State which parasite is depicted.
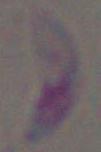
This is Toxoplasma gondii.

Summary:
  - Magnification: 1000x
  - Modality: photomicrograph